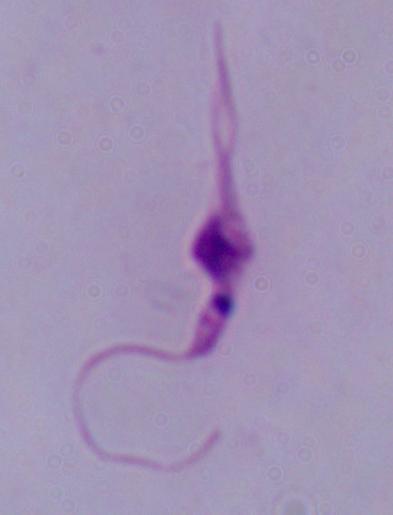

magnification = 1000x
modality = micrograph
identification = Leishmania